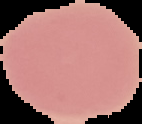
From a thin blood smear. Image is 142×124 pixels. Segmented cell region on a black background. Result: no malaria parasites detected.